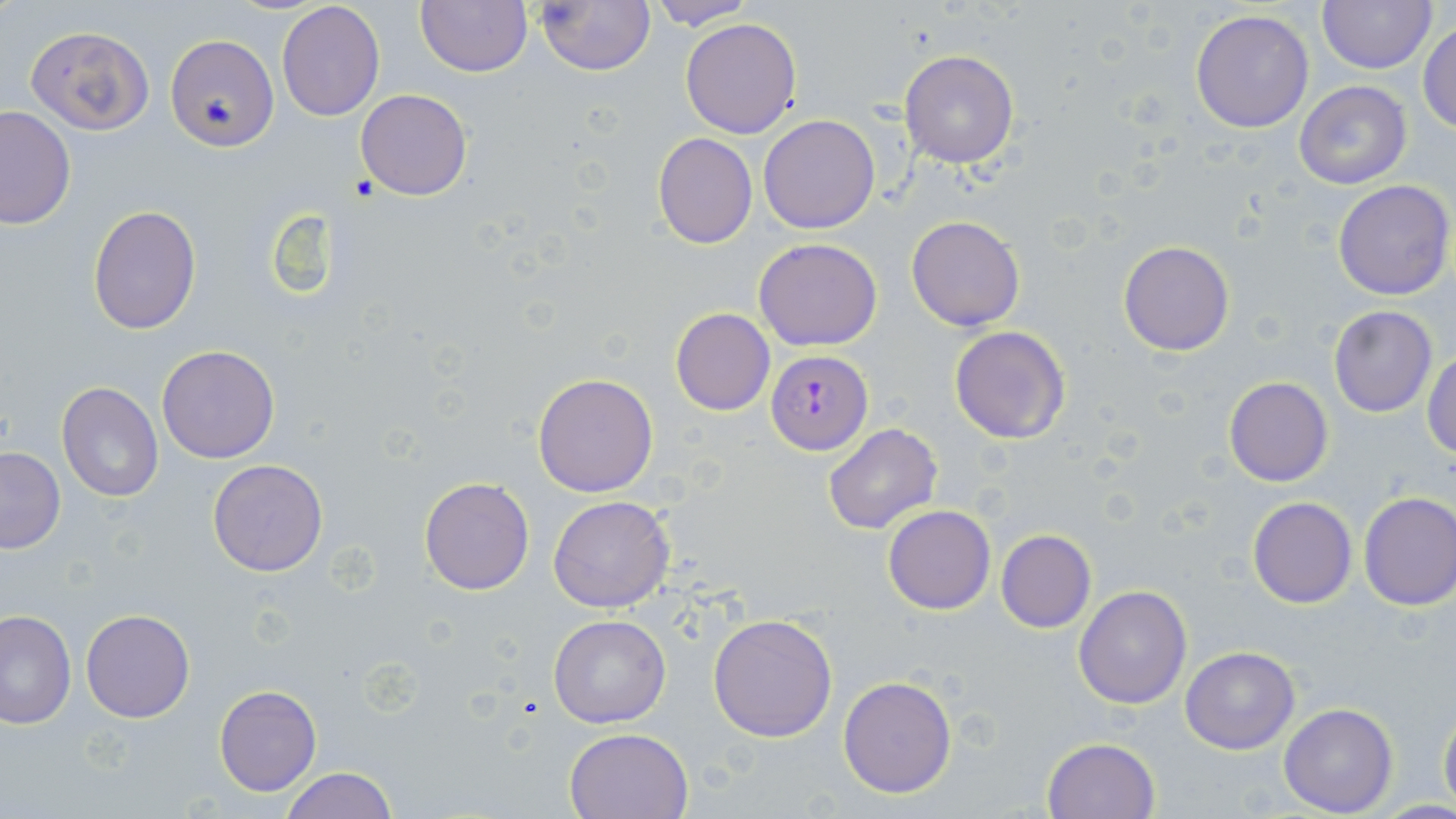

Approximate bounding boxes as named x1/y1/x2/y2 corners in pixels. Uninfected red blood cell locations: (x1=415, y1=0, x2=531, y2=75), (x1=535, y1=0, x2=656, y2=77), (x1=645, y1=0, x2=758, y2=29), (x1=1317, y1=0, x2=1437, y2=73), (x1=276, y1=1, x2=385, y2=121), (x1=1190, y1=8, x2=1313, y2=133), (x1=679, y1=17, x2=803, y2=138), (x1=1418, y1=21, x2=1456, y2=135), (x1=26, y1=26, x2=154, y2=134), (x1=167, y1=34, x2=278, y2=150), (x1=898, y1=49, x2=1019, y2=169), (x1=1292, y1=80, x2=1413, y2=189), (x1=357, y1=89, x2=471, y2=201), (x1=0, y1=106, x2=75, y2=230), (x1=759, y1=114, x2=880, y2=235), (x1=653, y1=132, x2=757, y2=248), (x1=1331, y1=180, x2=1455, y2=300), (x1=88, y1=203, x2=200, y2=334), (x1=906, y1=215, x2=1027, y2=331), (x1=754, y1=238, x2=882, y2=351), (x1=1118, y1=240, x2=1235, y2=356), (x1=1328, y1=305, x2=1437, y2=417), (x1=670, y1=308, x2=775, y2=416), (x1=949, y1=325, x2=1071, y2=445), (x1=156, y1=345, x2=281, y2=464), (x1=1424, y1=353, x2=1456, y2=460), (x1=533, y1=373, x2=658, y2=497), (x1=1224, y1=377, x2=1333, y2=486), (x1=56, y1=380, x2=164, y2=503), (x1=822, y1=423, x2=943, y2=534), (x1=0, y1=447, x2=66, y2=554), (x1=206, y1=459, x2=330, y2=577), (x1=419, y1=477, x2=535, y2=595), (x1=1357, y1=492, x2=1456, y2=611), (x1=548, y1=494, x2=674, y2=612), (x1=1248, y1=496, x2=1357, y2=609), (x1=884, y1=505, x2=996, y2=615), (x1=995, y1=529, x2=1096, y2=632), (x1=1074, y1=585, x2=1193, y2=709), (x1=0, y1=608, x2=75, y2=728), (x1=81, y1=609, x2=196, y2=722), (x1=548, y1=613, x2=672, y2=729), (x1=708, y1=613, x2=837, y2=741), (x1=1180, y1=646, x2=1300, y2=753), (x1=838, y1=676, x2=957, y2=798), (x1=213, y1=685, x2=322, y2=796), (x1=1438, y1=700, x2=1456, y2=812), (x1=1280, y1=703, x2=1398, y2=816), (x1=564, y1=726, x2=694, y2=818), (x1=1042, y1=737, x2=1162, y2=819), (x1=277, y1=766, x2=399, y2=819). Plasmodium falciparum-infected red blood cell locations: (x1=766, y1=350, x2=873, y2=455). Slide-level diagnosis: Plasmodium falciparum. 1000x magnification. Single field of view. Thin blood smear. Image is 1456×819 pixels. Light microscopy. May-Grünwald-Giemsa stain.